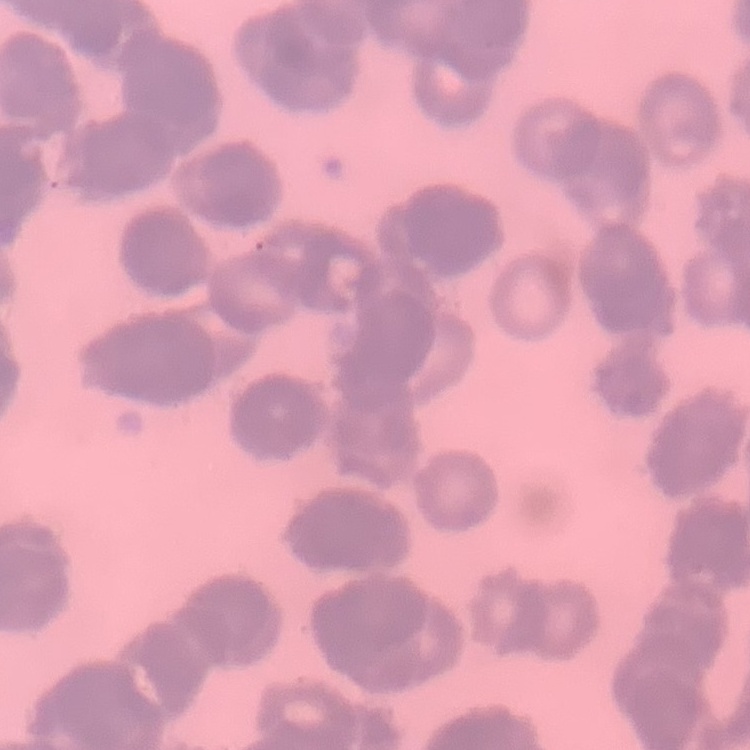
erythrocyte morphology = rouleaux formation
stain = Field's or Giemsa
image type = square crop of a larger photomicrograph
preparation = thin peripheral smear